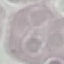

result = no malaria parasites detected
preparation = thin blood smear
stain = Giemsa
image type = cell patch, automatically extracted from a larger field of view and resized to 64 × 64 pixels
capture = smartphone through the microscope eyepiece